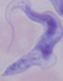
A trypanosome is shown. 1000x magnification. Micrograph.